Name the parasite shown.
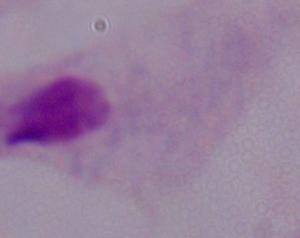
This is a trichomonad.

magnification = 1000x
modality = photomicrograph